Classify this cell by malaria status.
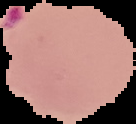
Parasitized.

preparation = thin blood film
image type = cell region segmented out of the field of view; surrounding area masked to black
image size = 136×124 pixels